Assess this cell for malaria.
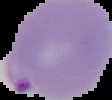
Parasitized.

Summary:
  - Image type: segmented cell region with the area outside set to black
  - Image size: 112×100 pixels
  - Preparation: thin blood film